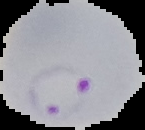
image_size: 145×130 pixels
image_type: cell region segmented out of the field of view; surrounding area masked to black
preparation: thin blood film
result: Plasmodium parasites detected